Identify the parasite.
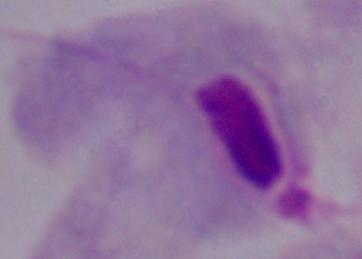

A trichomonad.

Summary:
  - Modality: photomicrograph
  - Magnification: 1000x